Assess this cell for malaria.
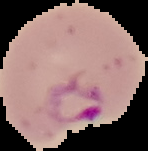

It is parasitized.

preparation = thin blood film
image type = segmented cell region with the area outside set to black
image size = 148×151 pixels